Name the parasite shown.
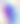
Toxoplasma gondii.

modality = photomicrograph
magnification = 400x